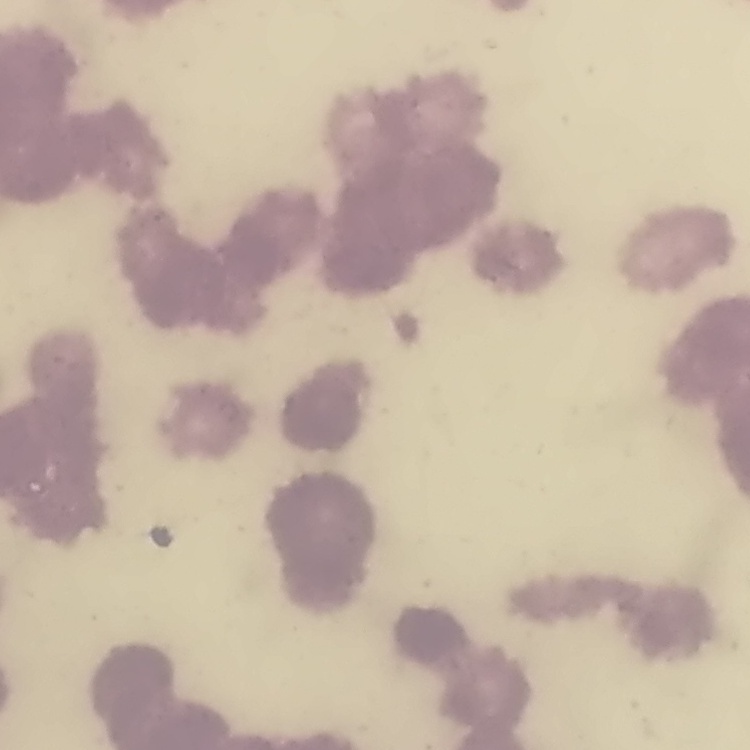
{
  "erythrocyte_morphology": "rouleaux formation",
  "preparation": "thin blood film",
  "stain": "Field's or Giemsa",
  "image_type": "one tile cut from a larger photomicrograph"
}